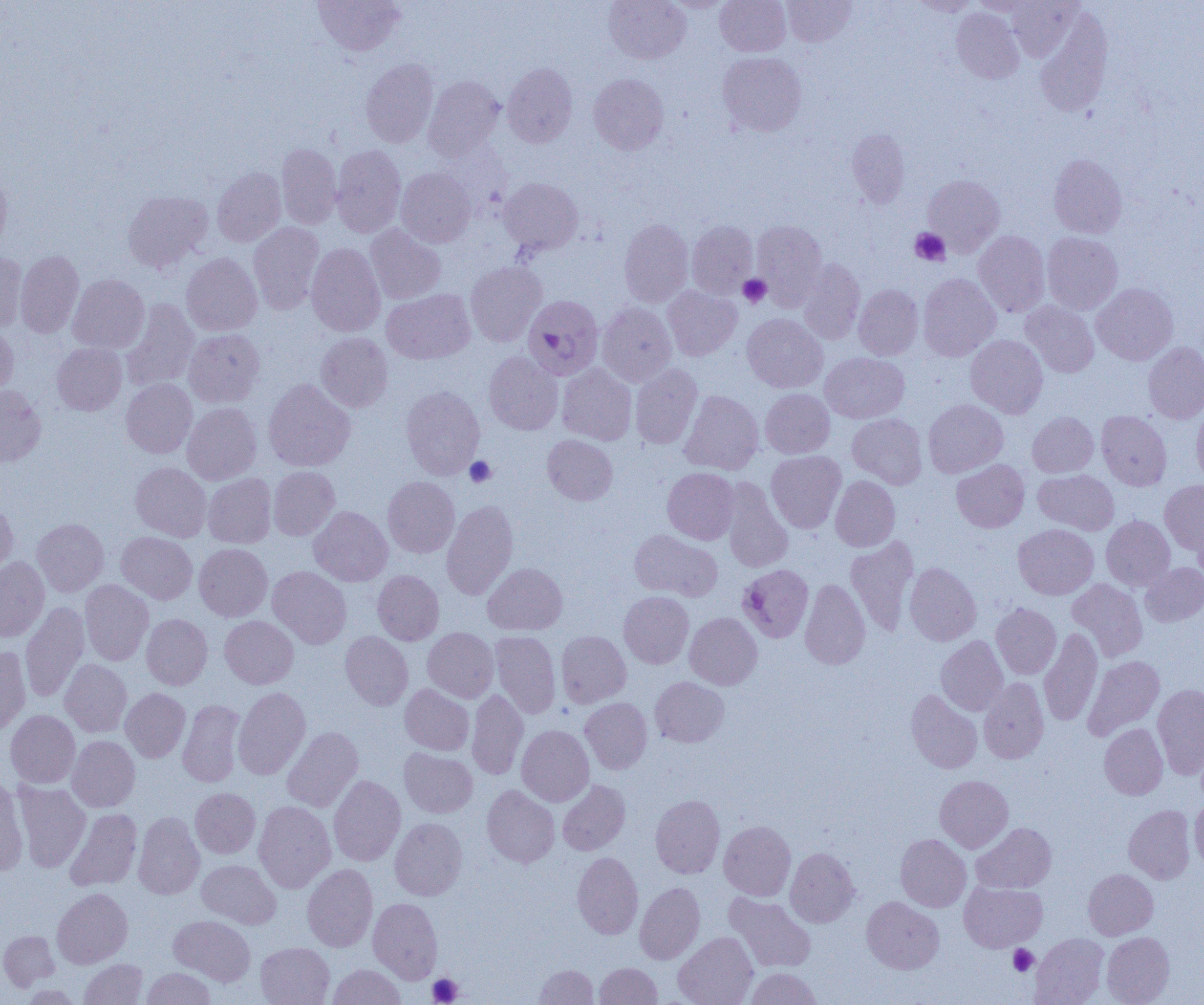
Plasmodium falciparum-infected red blood cell locations = approximate bounding boxes as (x1,y1)-(x2,y2) corner pairs in pixels: (523,295)-(603,380), (738,564)-(814,642)
slide-level diagnosis = Plasmodium falciparum
uninfected red blood cell locations = approximate bounding boxes as (x1,y1)-(x2,y2) corner pairs in pixels: (313,0)-(405,55), (604,0)-(691,63), (716,0)-(790,56), (781,0)-(856,46), (909,0)-(980,16), (969,0)-(1042,16), (1006,0)-(1084,61), (663,1)-(732,12), (952,7)-(1024,84), (1035,7)-(1113,117), (717,51)-(807,136), (360,58)-(439,147), (502,63)-(577,147), (588,73)-(668,154), (423,75)-(504,160), (846,129)-(910,207), (276,143)-(341,229), (331,145)-(406,237), (1048,154)-(1127,238), (212,167)-(286,246), (396,167)-(476,247), (0,171)-(11,253), (923,174)-(1004,255), (498,178)-(583,255), (123,190)-(213,272), (619,217)-(693,307), (752,220)-(827,306), (687,221)-(757,297), (248,223)-(323,314), (366,225)-(446,304), (973,230)-(1050,316), (1042,232)-(1123,314), (306,243)-(385,336), (15,249)-(84,338), (0,250)-(28,333), (181,252)-(262,335), (798,258)-(865,345), (465,261)-(546,346), (918,273)-(1001,361), (68,274)-(149,354), (854,283)-(923,359), (1092,283)-(1178,365), (663,286)-(741,360), (382,289)-(475,364), (120,299)-(199,391), (1020,301)-(1099,377), (597,302)-(676,386), (742,314)-(827,393), (0,322)-(18,397), (184,329)-(265,407), (316,332)-(393,412), (966,335)-(1048,418), (1143,342)-(1204,423), (52,343)-(127,415), (484,351)-(563,434), (820,352)-(909,423), (557,364)-(636,444), (630,365)-(702,448), (121,379)-(197,458), (264,379)-(355,472), (0,385)-(46,467), (401,386)-(485,479), (761,389)-(834,458), (679,390)-(763,474), (923,399)-(1008,477), (182,403)-(261,484), (1192,404)-(1204,486), (1096,411)-(1172,490), (1027,412)-(1098,477), (848,413)-(927,489), (543,435)-(617,505), (766,450)-(846,533), (951,459)-(1029,532), (130,462)-(211,541), (268,466)-(340,540), (663,468)-(740,544), (1034,469)-(1118,535), (203,474)-(276,548), (383,476)-(459,557), (830,476)-(900,551), (722,480)-(793,572), (1160,480)-(1204,555), (0,500)-(18,579), (441,500)-(518,600), (309,506)-(392,586), (1101,515)-(1175,590), (32,518)-(109,596), (1194,519)-(1204,584), (1013,524)-(1098,599), (629,529)-(721,601), (116,531)-(197,604), (845,537)-(918,636), (194,543)-(272,621), (0,557)-(49,641), (904,562)-(981,645), (1140,562)-(1204,626), (483,563)-(567,635), (267,566)-(351,649), (373,570)-(444,645), (80,579)-(153,665), (800,579)-(870,669), (1067,579)-(1147,661), (619,591)-(693,668), (20,602)-(89,703), (991,603)-(1061,678), (685,612)-(762,689), (141,613)-(212,690), (219,615)-(298,688), (423,627)-(498,702), (1039,627)-(1103,727), (556,630)-(631,707), (340,631)-(413,710), (491,631)-(561,718), (936,636)-(1008,716), (0,647)-(31,734), (1083,655)-(1164,740), (60,659)-(132,737), (650,676)-(729,747), (979,677)-(1049,764), (1152,683)-(1204,778), (400,684)-(473,755), (233,687)-(311,779), (120,688)-(190,762), (466,689)-(528,780), (906,690)-(982,773), (580,698)-(652,774), (177,699)-(245,786), (5,710)-(80,788), (1099,723)-(1168,799), (516,725)-(594,806), (282,726)-(363,812), (67,736)-(140,811), (399,747)-(478,817), (329,775)-(405,866), (935,775)-(1013,852), (0,778)-(28,875), (558,780)-(630,855), (13,781)-(90,872), (482,785)-(559,868), (190,788)-(260,858), (650,794)-(725,878), (1190,800)-(1204,874), (254,801)-(335,892), (1124,805)-(1196,883), (65,807)-(142,891), (133,811)-(205,899), (390,817)-(467,900), (719,820)-(796,900), (971,823)-(1056,893), (895,834)-(971,912), (785,847)-(860,927), (572,852)-(643,939), (197,860)-(281,928), (302,864)-(377,952), (1083,868)-(1158,940), (959,881)-(1047,951), (635,882)-(705,964), (52,888)-(132,968), (725,893)-(815,972), (862,896)-(944,973), (368,897)-(442,983), (170,915)-(255,985), (0,930)-(60,991), (674,932)-(757,1005), (1102,932)-(1174,1004), (1031,933)-(1108,1005), (256,942)-(334,1005), (79,958)-(148,1005), (595,962)-(662,1005), (534,963)-(598,1005), (328,964)-(406,1005), (142,968)-(216,1004), (745,968)-(822,1005)
field of view = single
magnification = 1000x
platelet locations = approximate bounding boxes as (x1,y1)-(x2,y2) corner pairs in pixels: (910,228)-(950,266), (738,274)-(771,307), (465,456)-(496,487), (1008,944)-(1038,976), (427,973)-(463,1004)
modality = light microscopy
preparation = thin blood smear
image size = 1204×1005 pixels